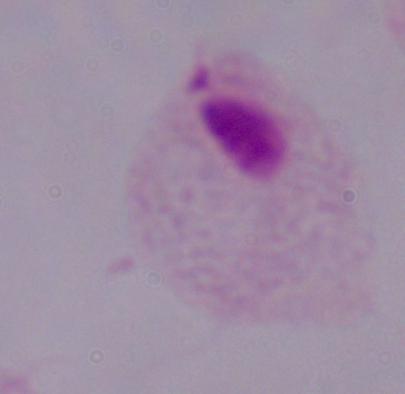
1000x magnification. Micrograph. A trichomonad is seen.